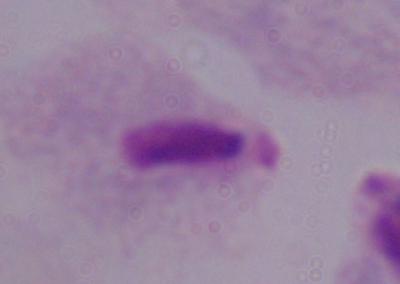

{
  "identification": "trichomonad",
  "magnification": "1000x",
  "modality": "photomicrograph"
}